Point out each leukocyte.
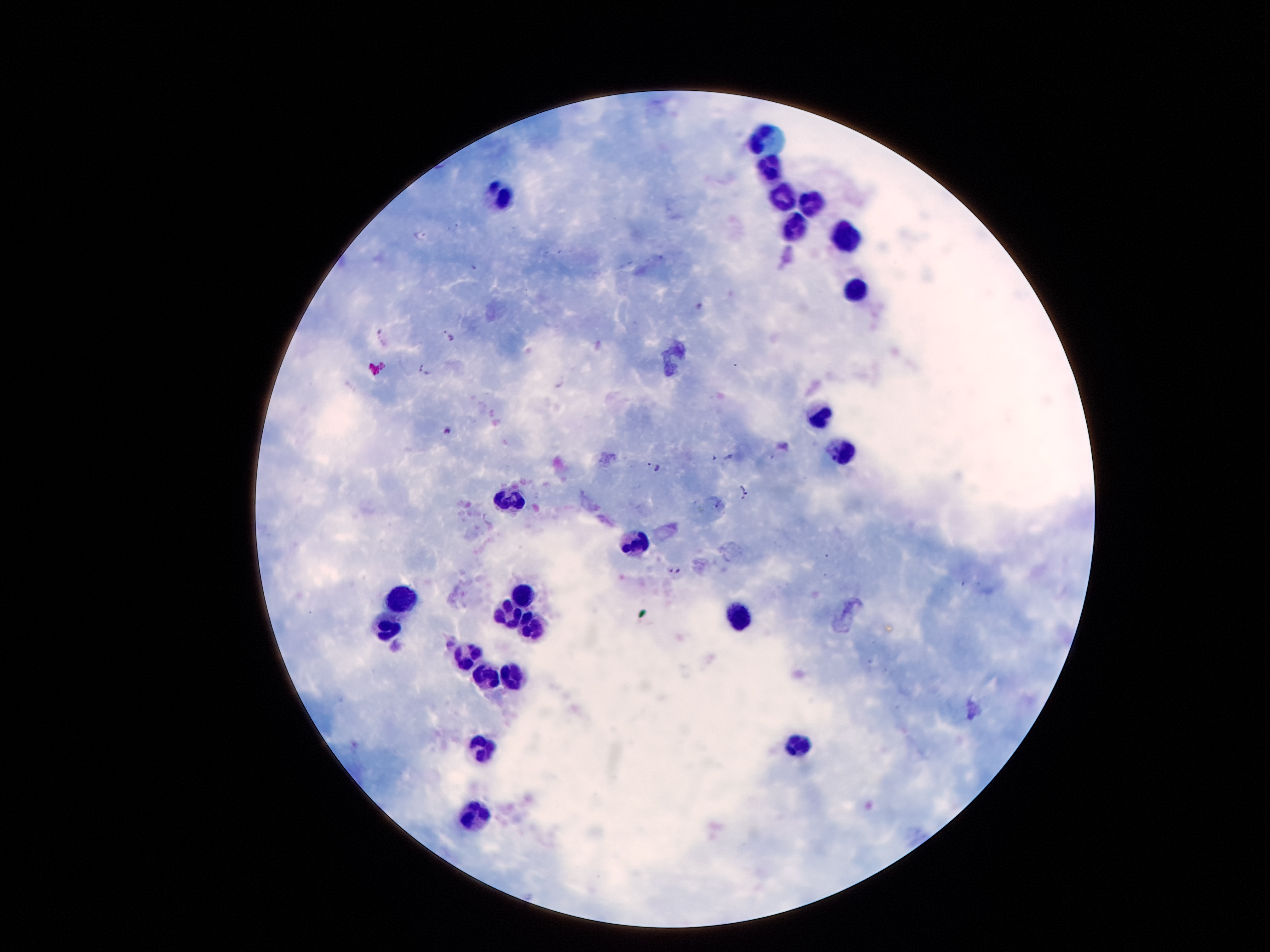
Approximate centers as [x, y] in pixels.
Leukocytes: [769, 137], [775, 169], [781, 197], [506, 198], [811, 204], [794, 227], [841, 233], [857, 287], [817, 416], [842, 453], [511, 503], [637, 539], [523, 595], [402, 600], [734, 615], [515, 618], [532, 625], [388, 629], [470, 658], [484, 680], [511, 680], [798, 749], [482, 750], [474, 817].

Plasmodium parasite locations = [422, 236], [383, 336], [450, 336], [426, 367], [448, 430], [729, 456], [714, 457], [655, 467], [744, 491], [676, 570]
stain = Giemsa
image size = 1270×952 pixels
capture = smartphone through the microscope eyepiece
patient malaria status = positive for Plasmodium falciparum
magnification = 100x
preparation = thick blood film
field of view = one from this slide